Locate every blood parasite and identify its species.
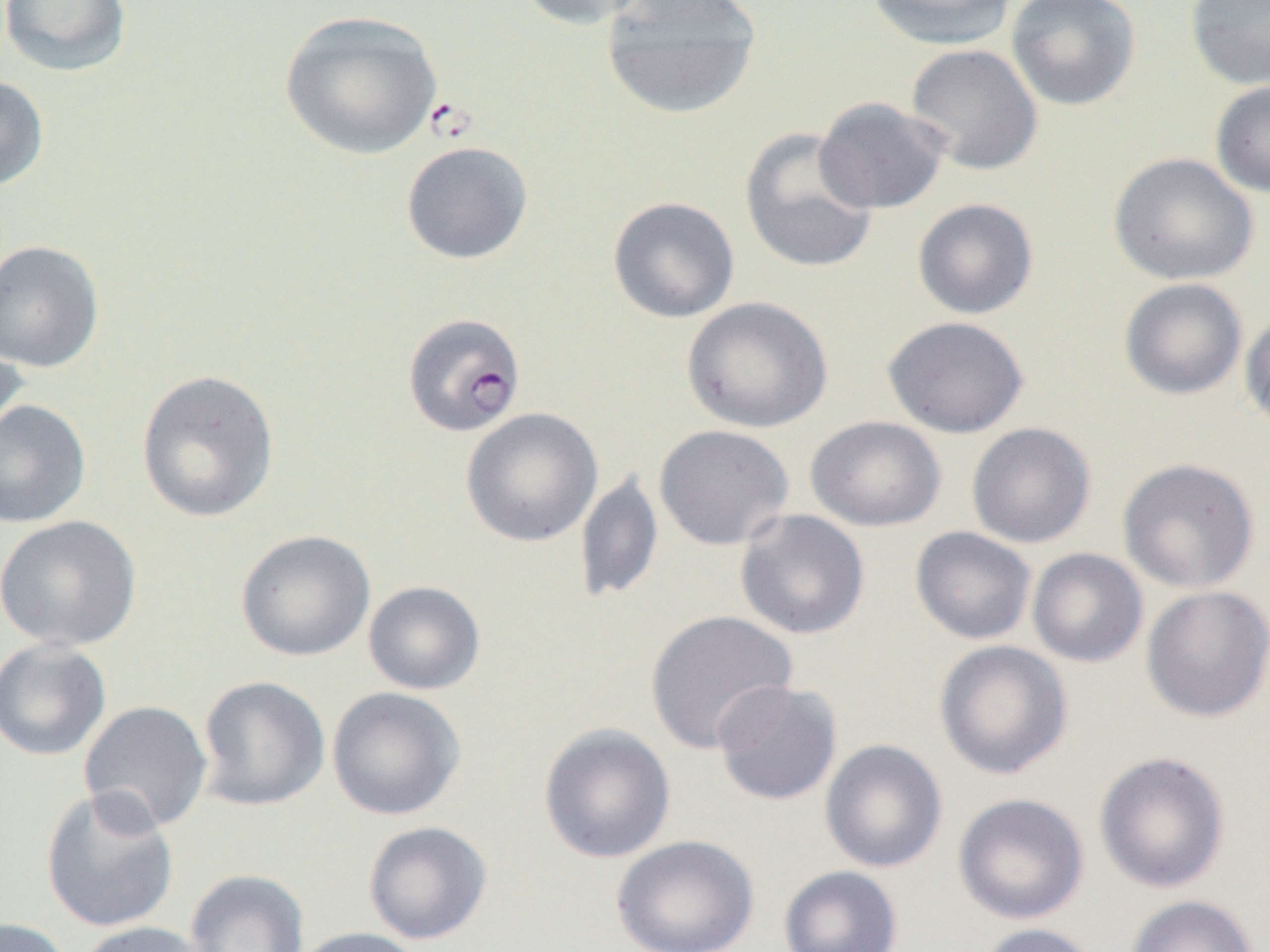
Approximate bounding boxes as [x1, y1, x2, y2] in pixels.
Plasmodium falciparum-infected red blood cells: [402, 312, 526, 437].
No Plasmodium ovale, Plasmodium malariae, Plasmodium vivax, Babesia divergens, or Trypanosoma brucei observed.

Summary:
  - Uninfected red blood cell locations: [1, 0, 132, 76], [514, 0, 652, 30], [600, 0, 763, 120], [866, 0, 1019, 50], [1006, 0, 1141, 111], [1185, 0, 1270, 91], [279, 10, 443, 160], [904, 43, 1043, 176], [0, 74, 49, 191], [1210, 80, 1270, 198], [813, 97, 951, 214], [739, 127, 879, 274], [400, 141, 533, 264], [1109, 152, 1259, 286], [607, 196, 740, 323], [912, 198, 1039, 319], [0, 240, 104, 373], [1118, 278, 1248, 400], [681, 296, 834, 433], [1240, 310, 1270, 434], [882, 315, 1030, 438], [0, 331, 29, 451], [136, 369, 280, 523], [0, 399, 91, 528], [460, 407, 603, 547], [806, 416, 947, 532], [966, 421, 1096, 548], [653, 424, 794, 550], [1117, 457, 1260, 594], [575, 469, 663, 605], [735, 509, 870, 640], [1, 515, 142, 651], [910, 526, 1037, 645], [235, 529, 376, 662], [1027, 547, 1148, 668], [363, 581, 486, 695], [1140, 585, 1270, 723], [644, 610, 798, 754], [0, 638, 111, 761], [933, 640, 1073, 780], [196, 675, 330, 812], [712, 679, 842, 806], [326, 686, 466, 821], [78, 700, 214, 834], [538, 722, 676, 863], [820, 739, 948, 873], [1094, 750, 1231, 893], [39, 786, 180, 934], [952, 792, 1089, 925], [363, 820, 492, 944], [612, 834, 760, 952], [779, 865, 903, 952], [185, 868, 310, 952], [1125, 894, 1261, 952], [0, 917, 72, 952], [75, 921, 211, 952], [976, 922, 1102, 952], [290, 926, 425, 952]
  - Slide-level diagnosis: Plasmodium falciparum
  - Preparation: thin blood film
  - Modality: optical microscopy
  - Field of view: single
  - Image size: 1270×952 pixels
  - Magnification: 1000x